Assess this cell for malaria.
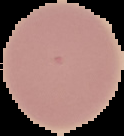
Uninfected.

Summary:
  - Preparation: thin blood smear
  - Image type: segmented cell region with the area outside set to black
  - Image size: 124×136 pixels